Comment on the morphology of the red blood cells.
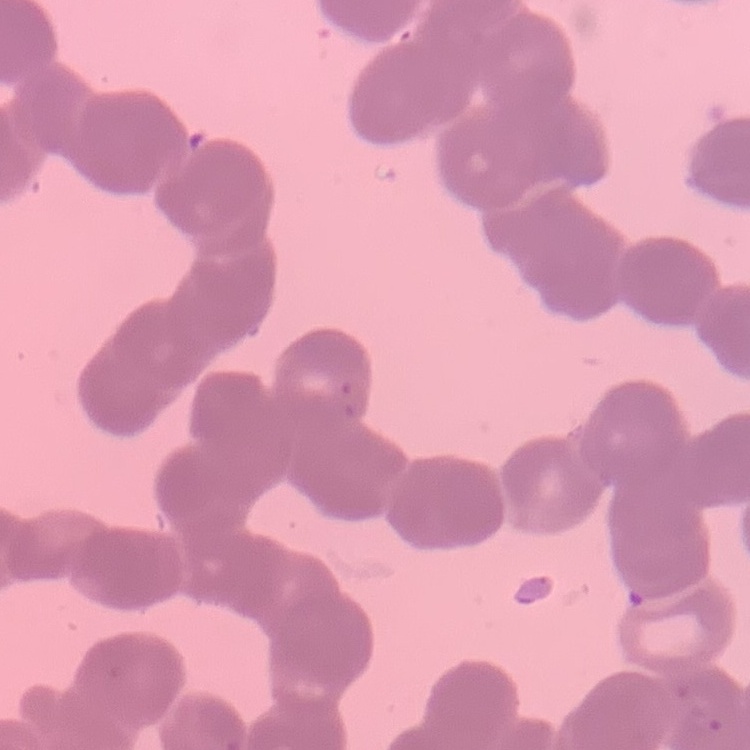
They show rouleaux formation.

Summary:
  - Preparation: thin blood smear
  - Stain: Field's or Giemsa
  - Image type: square crop of a larger photomicrograph